Locate and identify every blood parasite.
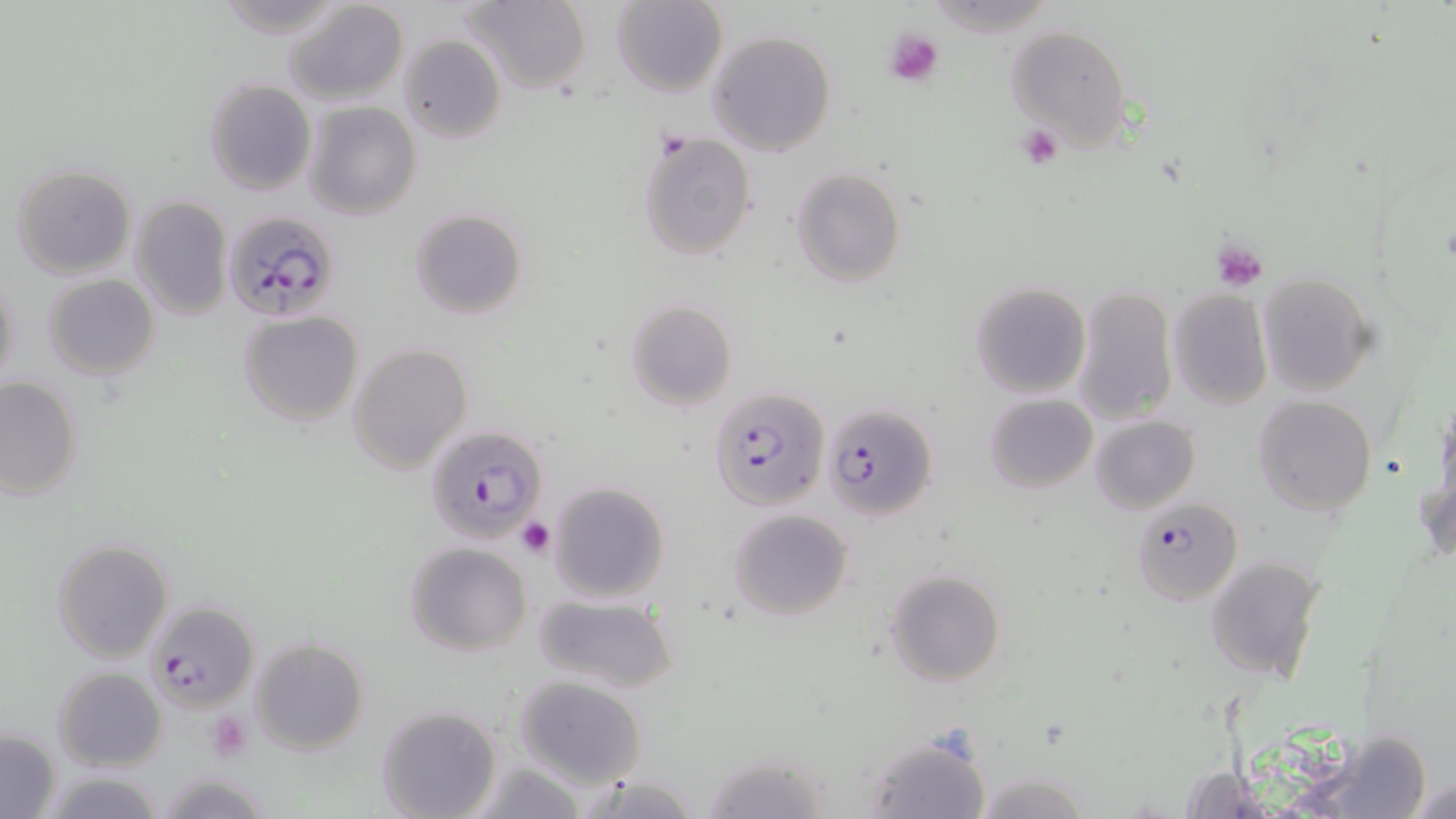
Approximate bounding boxes as (x1, y1, x2, y2) in pixels.
Plasmodium falciparum-infected red blood cells: (220, 209, 342, 322), (710, 387, 833, 512), (824, 401, 937, 521), (425, 423, 548, 544), (1132, 497, 1242, 606), (144, 599, 258, 714).
No Plasmodium ovale, Plasmodium malariae, Plasmodium vivax, Babesia divergens, or Trypanosoma brucei observed.

Uninfected red blood cell locations: (215, 0, 345, 34), (281, 0, 409, 106), (461, 0, 592, 95), (612, 0, 727, 96), (1005, 26, 1130, 151), (707, 29, 837, 157), (398, 35, 506, 144), (204, 80, 316, 197), (302, 100, 422, 221), (638, 131, 756, 261), (12, 165, 136, 279), (790, 166, 907, 287), (129, 196, 234, 320), (410, 208, 528, 319), (1257, 272, 1375, 395), (1, 273, 20, 393), (43, 273, 160, 381), (971, 281, 1091, 399), (1071, 284, 1179, 427), (1166, 289, 1273, 410), (626, 300, 737, 412), (237, 311, 363, 425), (347, 342, 474, 474), (0, 375, 84, 499), (986, 393, 1096, 492), (1253, 395, 1377, 516), (1435, 397, 1456, 512), (1090, 415, 1201, 514), (1416, 474, 1455, 567), (548, 480, 671, 603), (728, 508, 853, 619), (51, 537, 174, 664), (404, 542, 533, 655), (1204, 555, 1325, 684), (884, 569, 1005, 688), (532, 592, 678, 693), (249, 637, 369, 754), (52, 666, 167, 771), (512, 674, 647, 790), (377, 706, 502, 819), (1, 729, 60, 817), (1312, 731, 1433, 818), (863, 734, 990, 818), (704, 750, 832, 819), (468, 758, 588, 819), (1175, 764, 1271, 818), (36, 767, 167, 818), (154, 770, 276, 818), (972, 773, 1094, 817), (580, 774, 706, 817), (1406, 777, 1454, 818). Platelet locations: (885, 28, 945, 87), (1017, 125, 1064, 171), (1212, 240, 1269, 291), (516, 517, 554, 557), (207, 710, 254, 761). Slide-level diagnosis: Plasmodium falciparum. Thin blood smear. Image is 1456×819 pixels. Single field of view. 1000x magnification. Light microscopy. May-Grünwald-Giemsa-stained preparation.